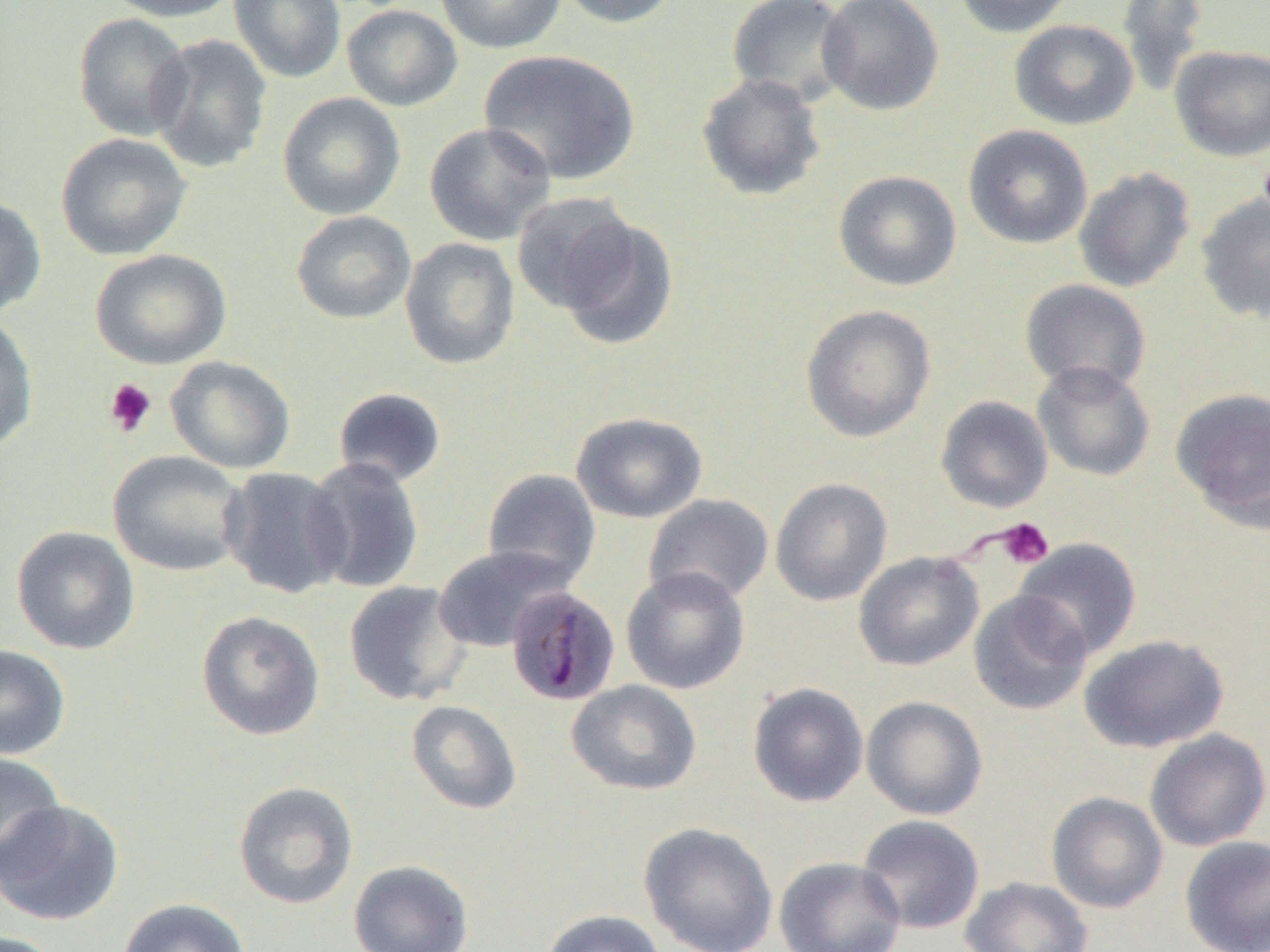 Approximate bounding boxes as named x1/y1/x2/y2 corners in pixels. Platelet locations: (x1=103, y1=378, x2=158, y2=438), (x1=995, y1=517, x2=1054, y2=569). Plasmodium malariae-infected red blood cell locations: (x1=506, y1=586, x2=620, y2=706). Uninfected red blood cell locations: (x1=100, y1=0, x2=241, y2=23), (x1=228, y1=0, x2=346, y2=84), (x1=435, y1=0, x2=566, y2=54), (x1=555, y1=0, x2=681, y2=29), (x1=727, y1=0, x2=854, y2=108), (x1=817, y1=0, x2=944, y2=116), (x1=953, y1=0, x2=1076, y2=38), (x1=1116, y1=0, x2=1209, y2=96), (x1=342, y1=4, x2=463, y2=111), (x1=72, y1=13, x2=193, y2=141), (x1=1009, y1=20, x2=1138, y2=130), (x1=148, y1=33, x2=272, y2=174), (x1=1169, y1=45, x2=1270, y2=161), (x1=478, y1=49, x2=640, y2=186), (x1=696, y1=72, x2=827, y2=202), (x1=277, y1=92, x2=406, y2=220), (x1=424, y1=122, x2=556, y2=246), (x1=962, y1=124, x2=1093, y2=249), (x1=56, y1=132, x2=192, y2=260), (x1=1073, y1=167, x2=1196, y2=293), (x1=832, y1=170, x2=962, y2=292), (x1=511, y1=192, x2=640, y2=317), (x1=1194, y1=192, x2=1270, y2=323), (x1=0, y1=195, x2=47, y2=317), (x1=290, y1=210, x2=416, y2=324), (x1=552, y1=215, x2=679, y2=351), (x1=399, y1=237, x2=520, y2=370), (x1=90, y1=248, x2=233, y2=370), (x1=1019, y1=279, x2=1151, y2=396), (x1=800, y1=304, x2=936, y2=442), (x1=0, y1=313, x2=39, y2=453), (x1=166, y1=356, x2=296, y2=474), (x1=1032, y1=360, x2=1156, y2=482), (x1=332, y1=387, x2=447, y2=488), (x1=1170, y1=387, x2=1270, y2=529), (x1=935, y1=395, x2=1053, y2=513), (x1=570, y1=411, x2=708, y2=524), (x1=108, y1=450, x2=248, y2=577), (x1=303, y1=457, x2=425, y2=594), (x1=219, y1=467, x2=351, y2=599), (x1=482, y1=468, x2=601, y2=588), (x1=770, y1=477, x2=892, y2=606), (x1=642, y1=494, x2=774, y2=608), (x1=10, y1=525, x2=141, y2=654), (x1=1012, y1=537, x2=1142, y2=661), (x1=431, y1=545, x2=574, y2=652), (x1=853, y1=551, x2=984, y2=671), (x1=620, y1=566, x2=751, y2=695), (x1=343, y1=580, x2=473, y2=706), (x1=969, y1=591, x2=1092, y2=716), (x1=196, y1=610, x2=325, y2=740), (x1=1078, y1=634, x2=1229, y2=753), (x1=0, y1=644, x2=71, y2=760), (x1=566, y1=680, x2=702, y2=795), (x1=747, y1=681, x2=869, y2=807), (x1=861, y1=696, x2=988, y2=820), (x1=405, y1=700, x2=522, y2=815), (x1=1145, y1=728, x2=1270, y2=851), (x1=0, y1=752, x2=66, y2=878), (x1=232, y1=780, x2=359, y2=909), (x1=1046, y1=791, x2=1168, y2=913), (x1=0, y1=798, x2=124, y2=926), (x1=856, y1=814, x2=985, y2=934), (x1=638, y1=821, x2=779, y2=952), (x1=1179, y1=835, x2=1270, y2=952), (x1=774, y1=856, x2=906, y2=952), (x1=348, y1=859, x2=474, y2=952), (x1=961, y1=876, x2=1093, y2=952), (x1=117, y1=898, x2=250, y2=952), (x1=539, y1=908, x2=666, y2=952), (x1=1, y1=931, x2=65, y2=952). Slide-level diagnosis: Plasmodium malariae. Image is 1270×952 pixels. Optical microscopy. One field of a larger specimen. Captured at 1000x magnification. Thin blood film.